Classify this cell by malaria status.
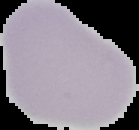
Uninfected.

Summary:
  - Preparation: thin blood smear
  - Image type: segmented cell region with the area outside set to black
  - Image size: 139×130 pixels